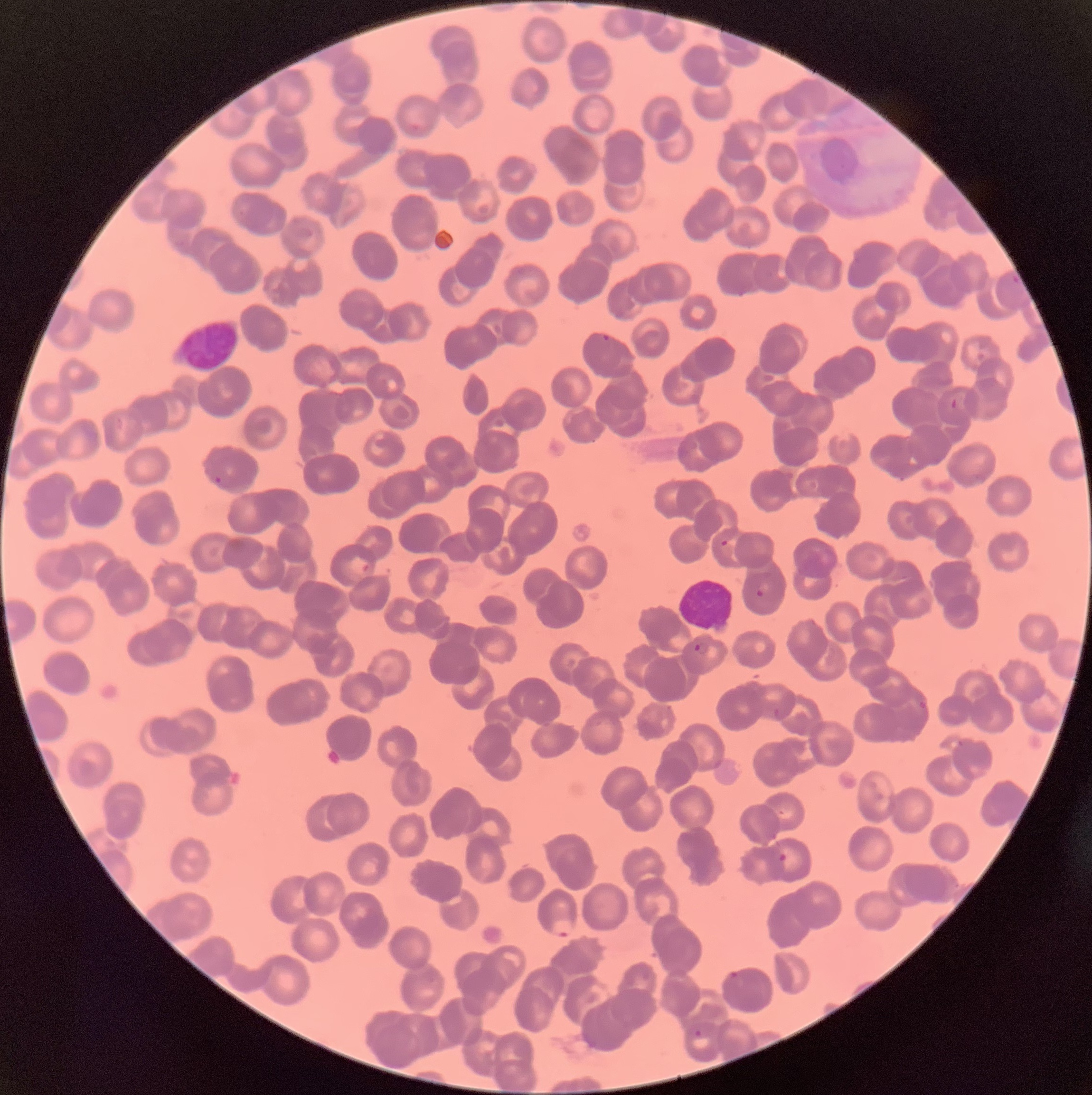

white_blood_cell_locations: 'approximate bounding boxes as (x1, y1, x2, y2) in pixels: (173, 316, 241, 371), (678, 574, 734, 632)'
preparation: thin blood film
plasmodium_parasite_locations: 'approximate bounding boxes as (x1, y1, x2, y2) in pixels: (600, 332, 611, 343), (950, 398, 958, 410), (213, 475, 223, 486), (720, 539, 729, 548), (756, 582, 771, 597), (694, 642, 709, 655), (914, 700, 928, 715), (777, 851, 788, 864), (550, 918, 575, 938), (724, 970, 741, 981), (692, 1029, 703, 1039)'
modality: optical microscopy
red_blood_cell_morphology: rouleaux formation
image_size: 1092×1095 pixels